Report the malaria status.
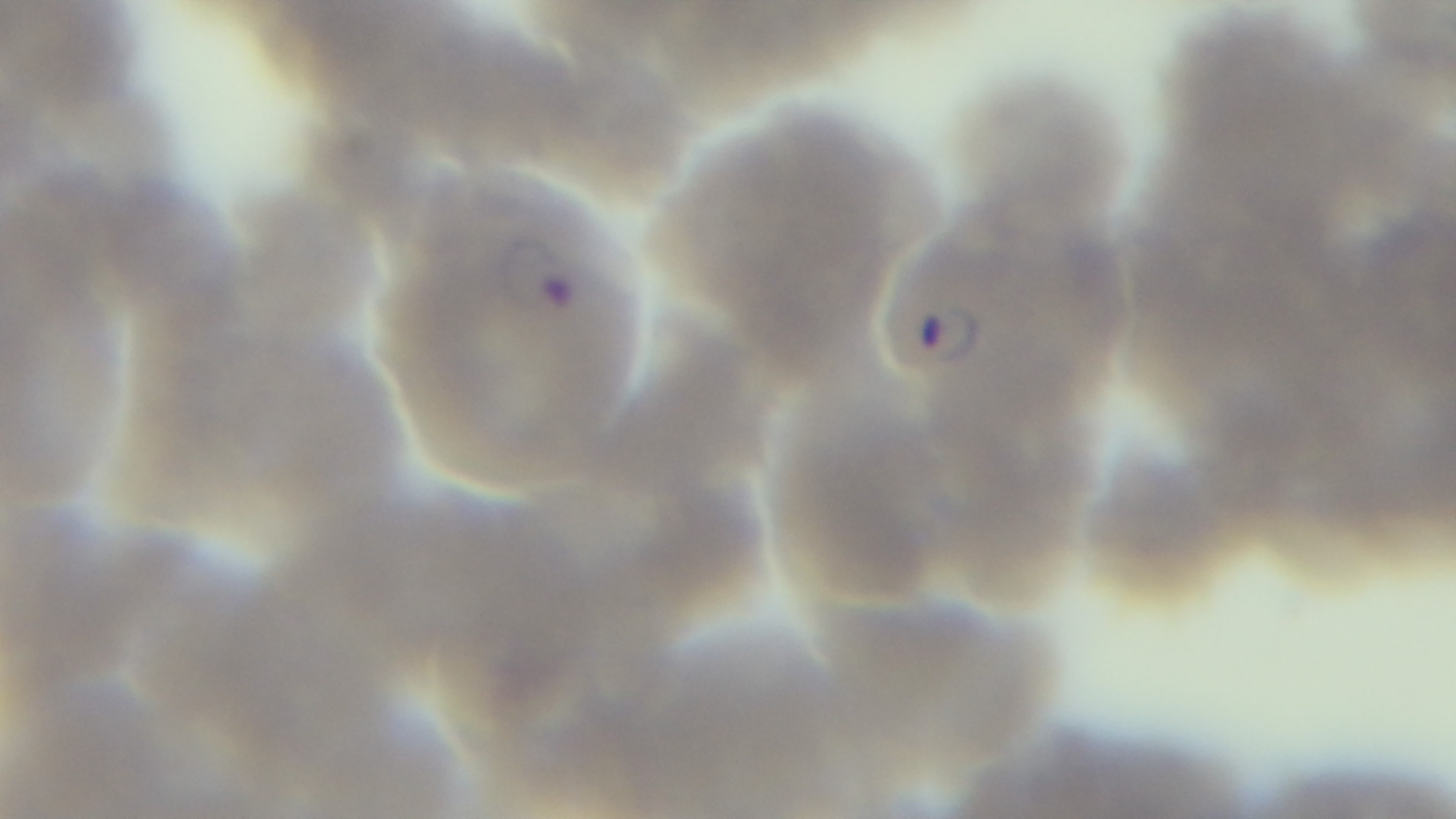
It is infected.

Summary:
  - Modality: light microscopy
  - Preparation: thin blood film
  - Objective: 100x oil immersion
  - Field of view: single
  - Stain: Giemsa
  - Capture: mounted 4K digital camera